Give the position of every malaria parasite.
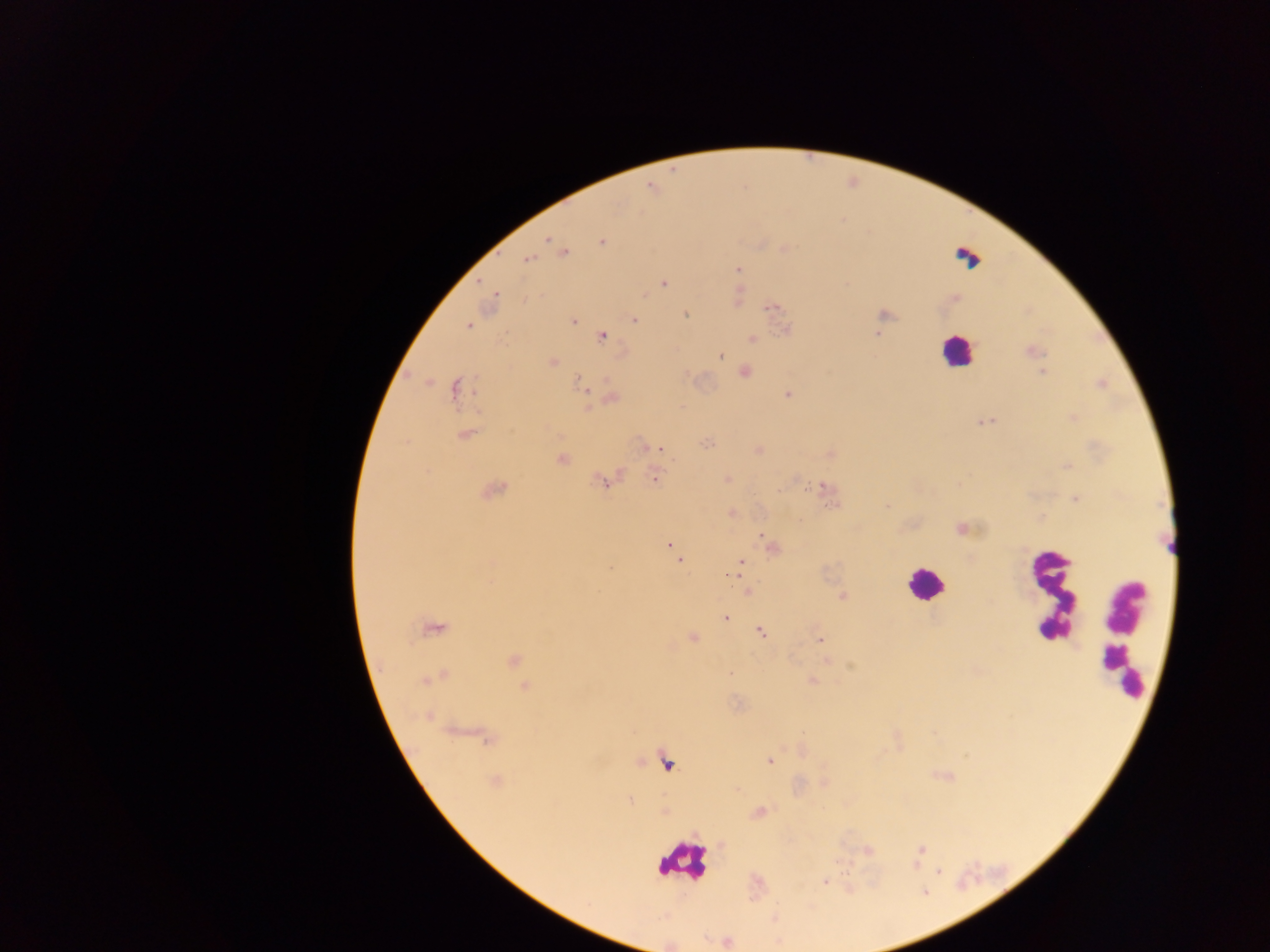

Approximate centers as x y in pixels.
Malaria parasites: 549 239; 602 241; 563 252; 527 260; 738 269; 663 284; 495 294; 772 307; 685 315; 634 319; 573 320; 469 325; 601 337; 720 356; 552 362; 745 372; 1043 373; 579 383; 456 388; 788 395; 612 398; 984 421; 466 434; 661 450; 561 459; 655 478; 601 483; 823 486; 494 491; 1076 499; 887 506; 761 536; 669 545; 679 560; 740 562; 732 575; 842 596; 725 618; 432 630; 761 632; 693 637; 820 640; 514 660; 430 679; 813 682; 525 686; 770 761; 495 781; 629 800; 921 850; 939 872; 825 881.

preparation = thick blood smear
field of view = single
country = Ghana
image size = 1270×952 pixels
capture = mobile-phone photograph through a microscope
leukocyte locations = approximate centers as x y in pixels: 968 253; 955 350; 925 584; 1051 593; 1123 637; 682 861